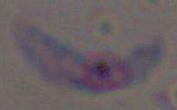

identification = Toxoplasma gondii
modality = photomicrograph
magnification = 1000x